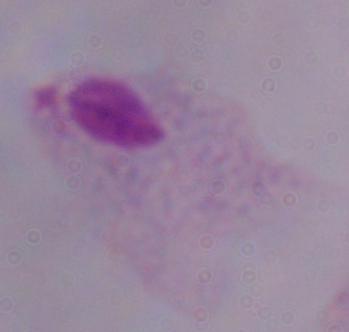

{
  "modality": "micrograph",
  "identification": "trichomonad",
  "magnification": "1000x"
}